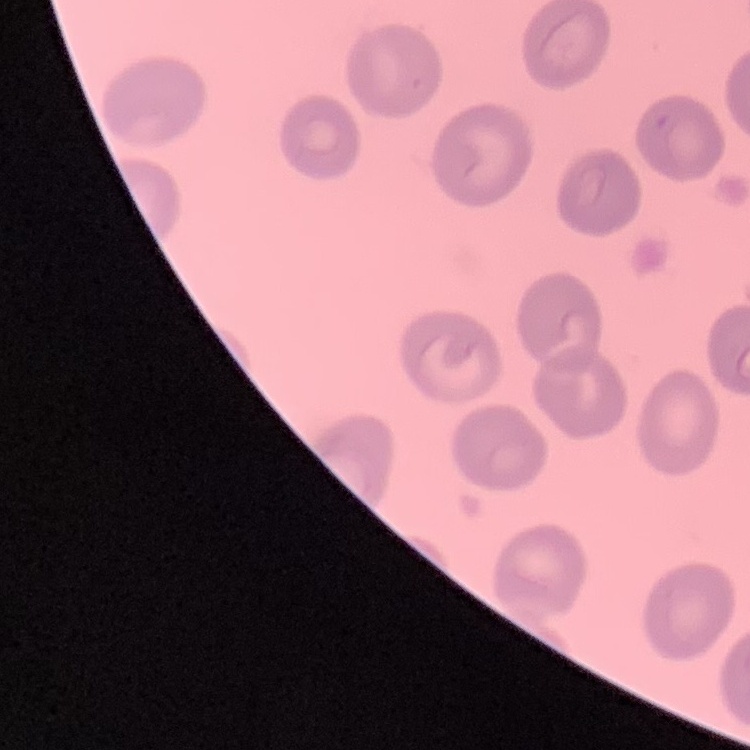

The erythrocytes show no rouleaux formation. Thin blood film. One tile cut from a larger photomicrograph. Stained with either Field's or Giemsa.